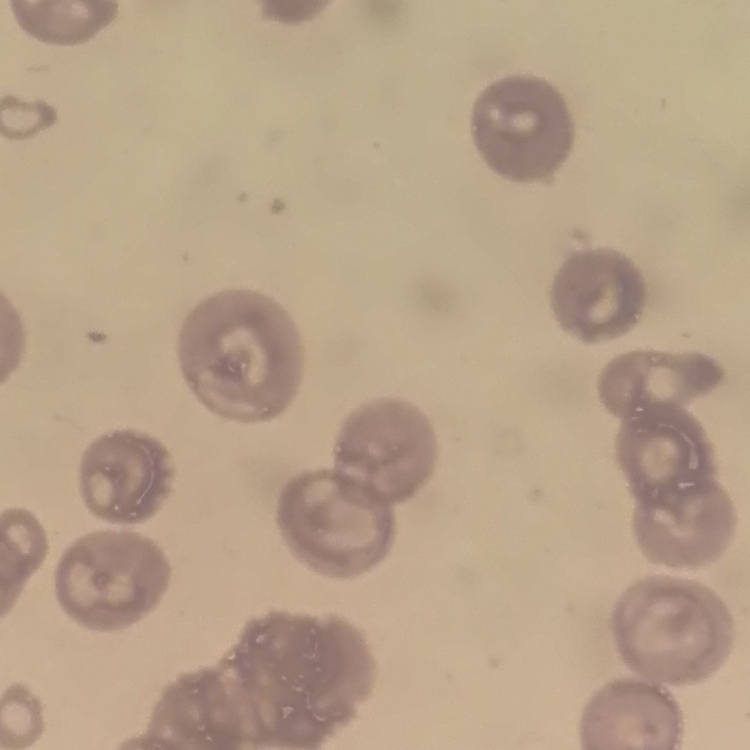 The erythrocytes exhibit no rouleaux formation. One tile cut from a larger photomicrograph. Thin blood smear. Stained with either Field's or Giemsa.